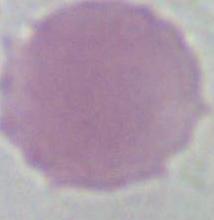

magnification = 1000x
identification = red blood cell
modality = photomicrograph